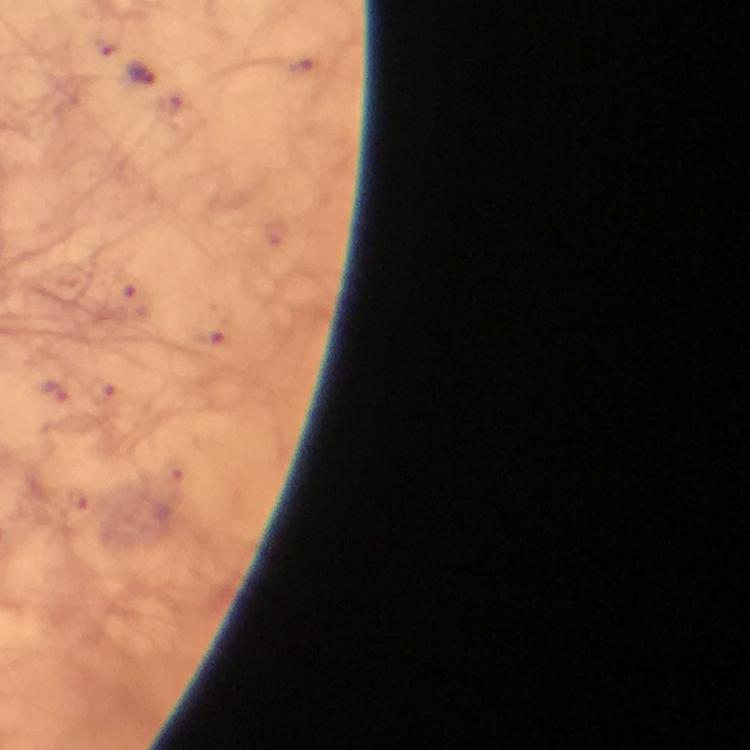
stain = Giemsa
immersion oil = used
cropped from = one field of view
Plasmodium parasite locations = approximate object centers, in pixels from the top-left corner: (x=140, y=73)
context = from a diagnostic examination for malaria
image size = 750×750 pixels
preparation = thick smear
magnification = 100x
capture = smartphone mounted on the microscope